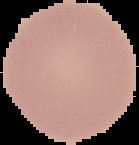

image type = segmented cell region on a black background
preparation = thin blood film
result = negative for Plasmodium parasites
image size = 139×145 pixels